Identify the parasite.
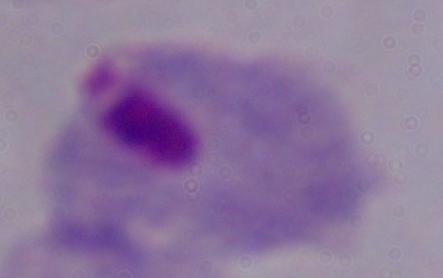

A trichomonad.

modality = micrograph
magnification = 1000x